Locate and identify every blood parasite.
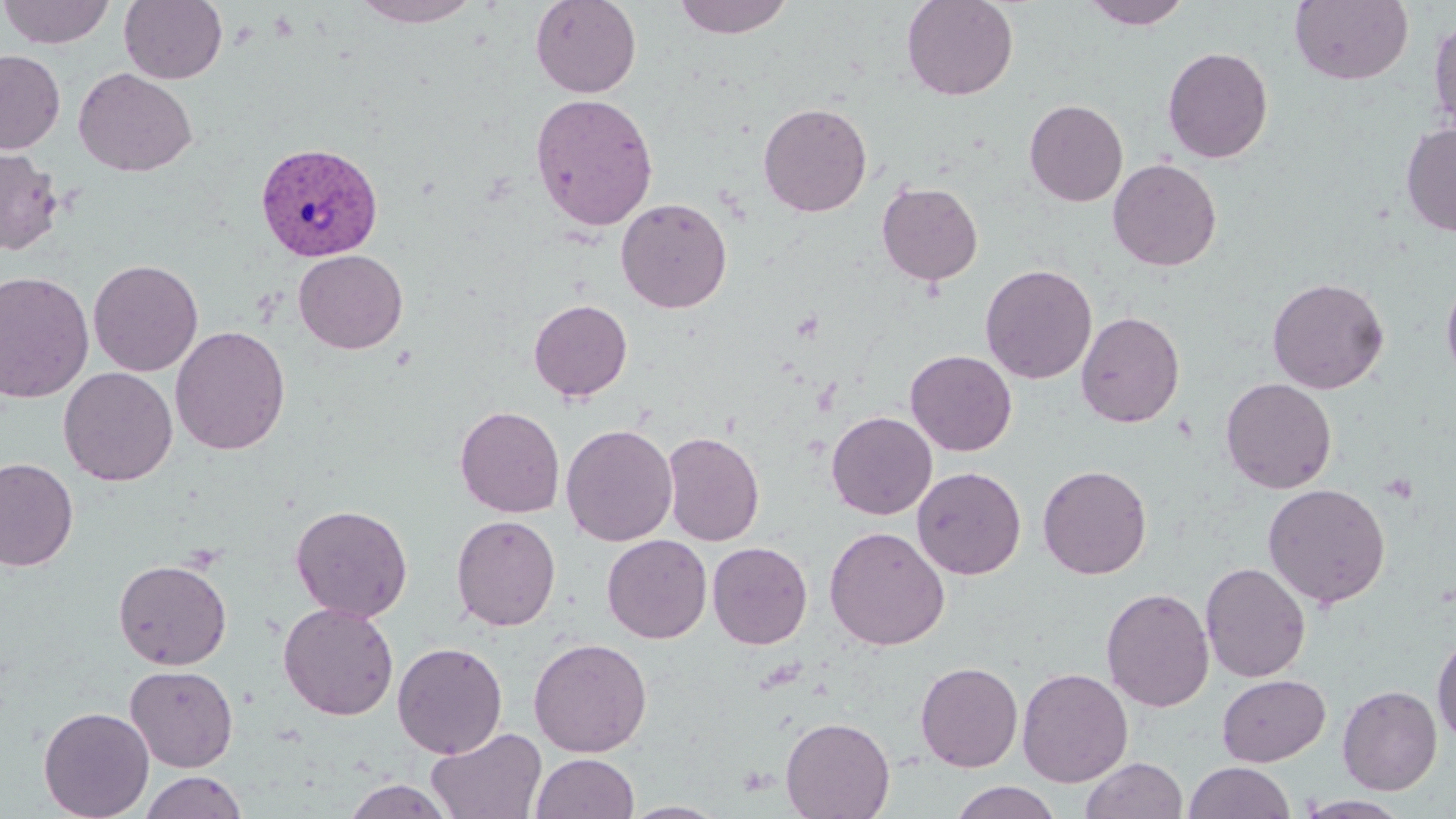
Approximate bounding boxes as (x1, y1, x2, y2) in pixels.
Plasmodium vivax-infected red blood cells: (254, 141, 384, 261).
No Plasmodium falciparum, Plasmodium ovale, Plasmodium malariae, Babesia divergens, or Trypanosoma brucei observed.

slide-level diagnosis = Plasmodium vivax
stain = May-Grünwald-Giemsa
field of view = single
uninfected red blood cell locations = approximate bounding boxes as (x1, y1, x2, y2) in pixels: (0, 0, 116, 49), (119, 0, 228, 84), (351, 0, 484, 27), (530, 0, 641, 98), (672, 0, 795, 40), (901, 0, 1019, 101), (1080, 0, 1192, 29), (1289, 0, 1414, 85), (1428, 12, 1456, 138), (1162, 47, 1273, 163), (0, 49, 65, 154), (73, 68, 197, 177), (530, 93, 659, 231), (1024, 99, 1128, 206), (758, 102, 873, 217), (1400, 122, 1456, 237), (0, 148, 63, 255), (1107, 158, 1222, 271), (877, 181, 983, 285), (616, 197, 733, 313), (293, 250, 408, 354), (88, 258, 203, 377), (980, 263, 1097, 384), (0, 270, 95, 403), (1441, 271, 1456, 388), (1267, 277, 1389, 394), (528, 299, 633, 401), (1076, 311, 1185, 428), (170, 325, 291, 455), (905, 350, 1017, 456), (58, 367, 177, 486), (1220, 378, 1337, 493), (455, 405, 565, 518), (826, 411, 937, 520), (561, 423, 678, 546), (662, 430, 765, 546), (0, 458, 78, 571), (1038, 464, 1153, 579), (912, 466, 1026, 580), (1262, 482, 1391, 608), (290, 503, 413, 622), (451, 514, 561, 631), (824, 526, 950, 650), (602, 534, 712, 643), (707, 541, 813, 649), (113, 558, 232, 670), (1201, 561, 1311, 682), (1101, 587, 1215, 711), (278, 602, 399, 720), (1432, 632, 1456, 745), (528, 637, 652, 757), (392, 641, 508, 758), (915, 661, 1023, 772), (125, 664, 239, 772), (1017, 667, 1134, 787), (1216, 673, 1331, 767), (1337, 684, 1442, 795), (38, 705, 155, 819), (780, 716, 896, 819), (426, 727, 547, 818), (531, 753, 639, 818), (1081, 757, 1187, 819), (1183, 761, 1297, 819), (138, 771, 249, 819), (341, 779, 457, 819), (948, 781, 1064, 819), (1296, 795, 1413, 818), (621, 801, 730, 818)
magnification = 1000x
modality = optical microscopy
image size = 1456×819 pixels
preparation = thin blood film